Report the malaria status of this cell.
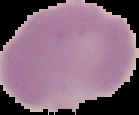

It is uninfected.

{
  "preparation": "thin blood film",
  "image_size": "139×115 pixels",
  "image_type": "cell region segmented out of the field of view; surrounding area masked to black"
}